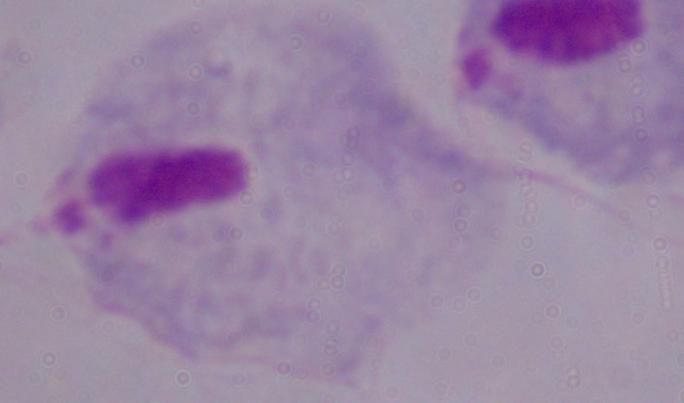

modality = micrograph
magnification = 1000x
identification = trichomonad